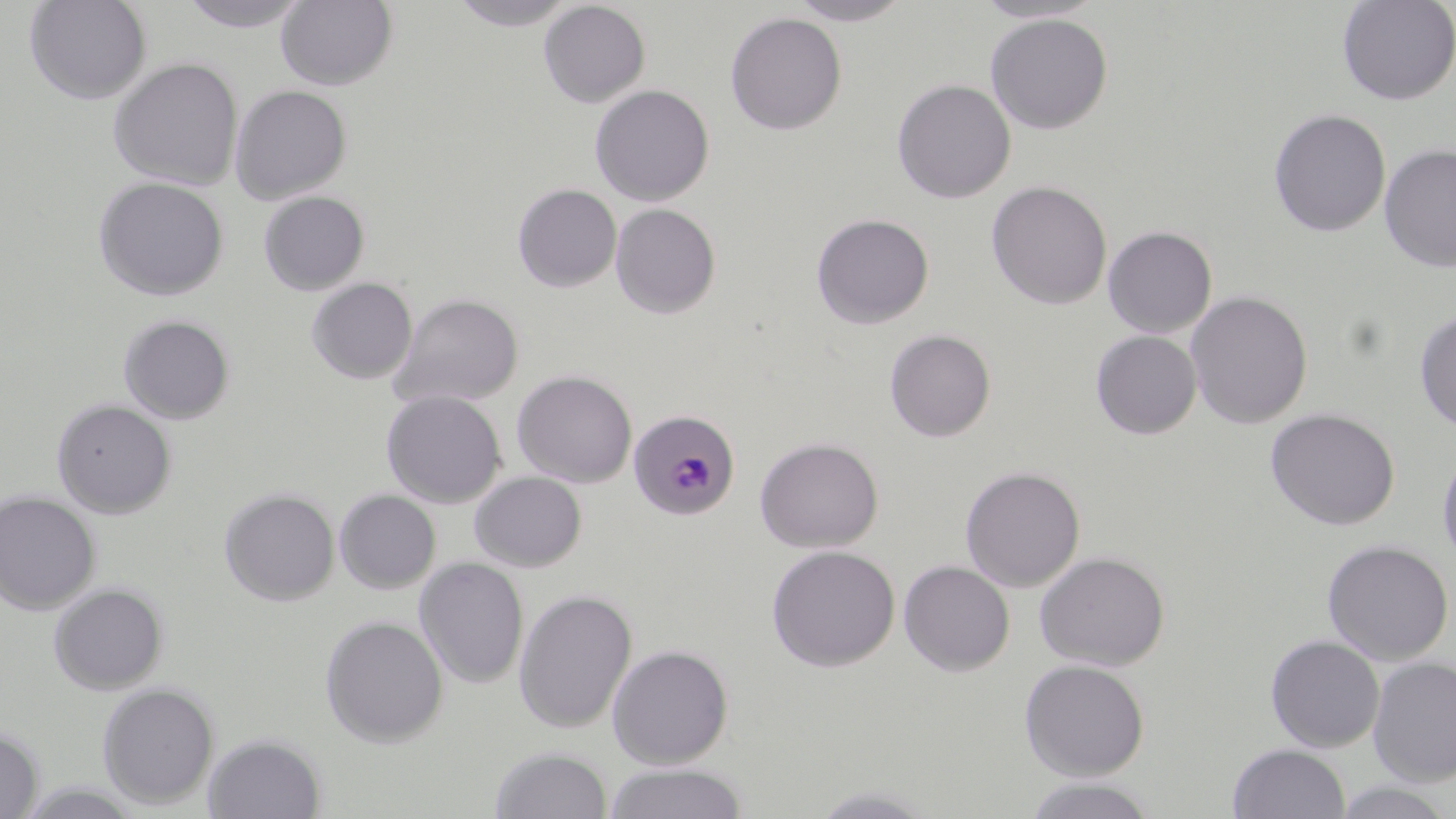 Approximate bounding boxes as (x1,y1)-(x2,y2) corner pairs in pixels. Uninfected red blood cell locations: (24,0)-(152,105), (179,0)-(310,32), (276,0)-(398,90), (448,0)-(577,30), (788,0)-(914,26), (972,0)-(1105,23), (1337,0)-(1456,106), (538,1)-(650,108), (724,11)-(847,135), (985,13)-(1113,134), (108,57)-(244,190), (891,79)-(1016,204), (590,84)-(714,206), (230,85)-(352,204), (1268,108)-(1391,237), (1379,143)-(1456,273), (93,176)-(229,301), (986,180)-(1112,310), (512,184)-(622,292), (258,191)-(370,295), (610,203)-(721,319), (811,213)-(934,329), (1102,226)-(1217,338), (307,278)-(417,384), (1186,291)-(1313,428), (389,293)-(524,409), (1414,309)-(1456,434), (118,315)-(236,424), (884,329)-(996,442), (1090,330)-(1202,439), (512,370)-(637,488), (381,390)-(507,508), (51,398)-(177,519), (1264,408)-(1400,530), (754,437)-(883,553), (1437,447)-(1456,569), (960,466)-(1086,592), (469,471)-(587,572), (220,488)-(339,606), (334,489)-(441,594), (0,492)-(101,614), (1322,539)-(1454,665), (766,544)-(901,672), (1035,551)-(1170,670), (414,558)-(529,689), (898,560)-(1015,676), (48,583)-(168,695), (513,588)-(637,734), (319,615)-(449,748), (1265,634)-(1385,752), (607,644)-(734,769), (1367,656)-(1456,786), (1019,659)-(1150,780), (96,682)-(220,810), (0,724)-(43,819), (203,733)-(326,818), (1228,743)-(1351,819), (490,746)-(613,819), (603,762)-(750,819), (1023,777)-(1159,819), (1332,781)-(1456,818), (807,785)-(942,818). Plasmodium malariae-infected red blood cell locations: (629,409)-(739,521). Slide-level diagnosis: Plasmodium malariae. 1000x magnification. One field of a larger specimen. Thin blood film. Light microscopy. Image is 1456×819 pixels. May-Grünwald-Giemsa stain.